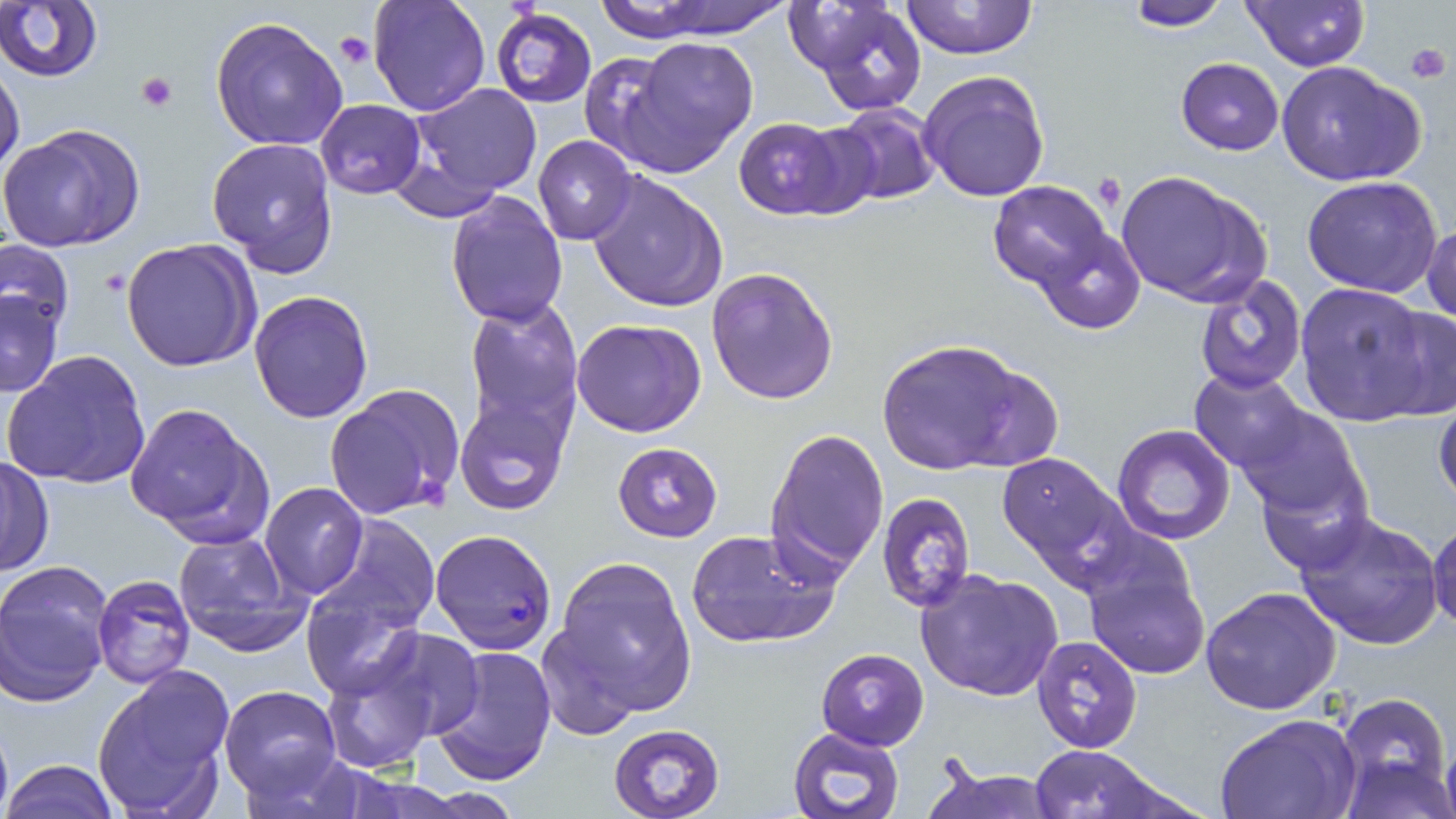
Summary:
  - Coordinate format: approximate bounding boxes as named x1/y1/x2/y2 corners in pixels
  - Uninfected red blood cell locations: (x1=368, y1=0, x2=489, y2=115), (x1=622, y1=0, x2=796, y2=43), (x1=898, y1=0, x2=1040, y2=59), (x1=1115, y1=0, x2=1231, y2=30), (x1=1239, y1=0, x2=1369, y2=71), (x1=793, y1=1, x2=927, y2=114), (x1=0, y1=3, x2=103, y2=83), (x1=490, y1=8, x2=596, y2=109), (x1=208, y1=17, x2=350, y2=153), (x1=623, y1=37, x2=758, y2=171), (x1=578, y1=51, x2=687, y2=169), (x1=0, y1=55, x2=24, y2=180), (x1=1175, y1=57, x2=1284, y2=156), (x1=1277, y1=60, x2=1426, y2=187), (x1=919, y1=71, x2=1050, y2=202), (x1=412, y1=83, x2=543, y2=200), (x1=316, y1=99, x2=425, y2=198), (x1=826, y1=104, x2=942, y2=205), (x1=733, y1=116, x2=855, y2=221), (x1=0, y1=122, x2=146, y2=253), (x1=533, y1=134, x2=638, y2=245), (x1=207, y1=137, x2=339, y2=276), (x1=587, y1=168, x2=728, y2=314), (x1=1113, y1=171, x2=1271, y2=309), (x1=1301, y1=176, x2=1444, y2=297), (x1=987, y1=181, x2=1115, y2=292), (x1=443, y1=189, x2=567, y2=328), (x1=1422, y1=221, x2=1456, y2=330), (x1=1033, y1=232, x2=1145, y2=335), (x1=0, y1=238, x2=75, y2=340), (x1=120, y1=240, x2=259, y2=373), (x1=704, y1=266, x2=839, y2=406), (x1=1193, y1=272, x2=1307, y2=395), (x1=1293, y1=282, x2=1441, y2=429), (x1=1, y1=286, x2=65, y2=398), (x1=248, y1=291, x2=374, y2=423), (x1=464, y1=298, x2=584, y2=438), (x1=1373, y1=304, x2=1456, y2=422), (x1=572, y1=318, x2=707, y2=438), (x1=874, y1=338, x2=1042, y2=477), (x1=4, y1=349, x2=152, y2=491), (x1=1188, y1=368, x2=1312, y2=478), (x1=1432, y1=385, x2=1456, y2=511), (x1=325, y1=386, x2=463, y2=523), (x1=453, y1=395, x2=569, y2=515), (x1=123, y1=400, x2=272, y2=542), (x1=1235, y1=405, x2=1368, y2=525), (x1=1112, y1=424, x2=1236, y2=546), (x1=766, y1=430, x2=889, y2=578), (x1=613, y1=442, x2=723, y2=541), (x1=995, y1=449, x2=1135, y2=592), (x1=0, y1=455, x2=54, y2=576), (x1=260, y1=483, x2=368, y2=600), (x1=876, y1=492, x2=976, y2=612), (x1=1293, y1=512, x2=1445, y2=651), (x1=322, y1=515, x2=441, y2=633), (x1=1429, y1=517, x2=1456, y2=633), (x1=686, y1=528, x2=841, y2=649), (x1=172, y1=529, x2=308, y2=656), (x1=1080, y1=542, x2=1213, y2=682), (x1=551, y1=555, x2=698, y2=716), (x1=1, y1=563, x2=113, y2=706), (x1=915, y1=568, x2=1066, y2=702), (x1=91, y1=574, x2=195, y2=689), (x1=302, y1=580, x2=426, y2=702), (x1=1200, y1=587, x2=1340, y2=717), (x1=535, y1=620, x2=643, y2=741), (x1=366, y1=626, x2=485, y2=742), (x1=1030, y1=635, x2=1144, y2=755), (x1=430, y1=645, x2=556, y2=785), (x1=815, y1=648, x2=929, y2=748), (x1=318, y1=657, x2=434, y2=772), (x1=92, y1=667, x2=235, y2=816), (x1=218, y1=684, x2=342, y2=801), (x1=1334, y1=692, x2=1452, y2=814), (x1=1215, y1=714, x2=1359, y2=819), (x1=608, y1=723, x2=726, y2=819), (x1=787, y1=726, x2=905, y2=819), (x1=1030, y1=745, x2=1164, y2=818), (x1=1, y1=759, x2=119, y2=818), (x1=922, y1=764, x2=1064, y2=819)
  - Plasmodium falciparum-infected red blood cell locations: (x1=429, y1=528, x2=558, y2=653)
  - Platelet locations: (x1=335, y1=32, x2=373, y2=69), (x1=1404, y1=42, x2=1451, y2=86), (x1=137, y1=74, x2=178, y2=112), (x1=1091, y1=172, x2=1123, y2=211)
  - Slide-level diagnosis: Plasmodium falciparum
  - Stain: May-Grünwald-Giemsa
  - Magnification: 1000x
  - Preparation: thin blood film
  - Image size: 1456×819 pixels
  - Modality: light microscopy
  - Field of view: single